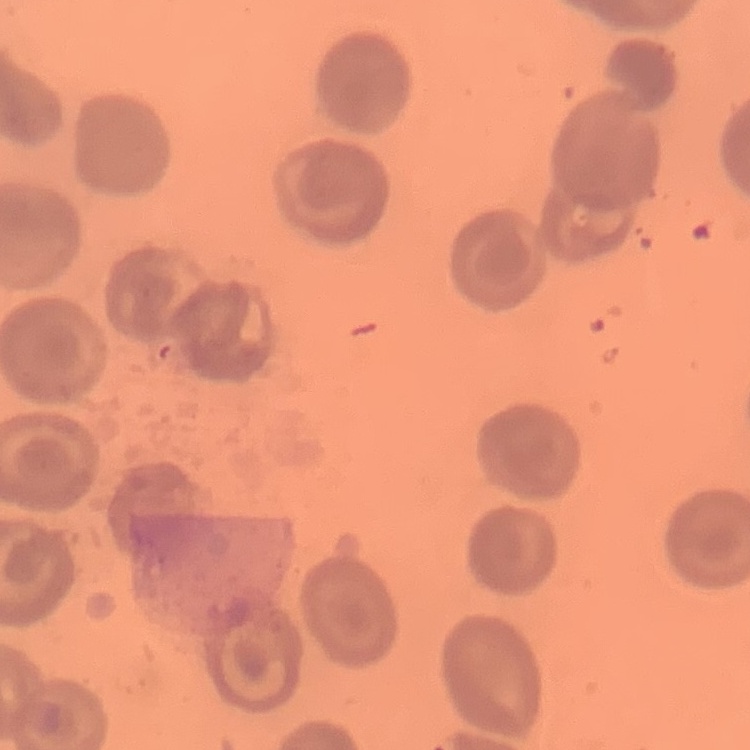

{
  "erythrocyte_morphology": "no rouleaux formation",
  "stain": "Field's or Giemsa",
  "image_type": "one tile cut from a larger photomicrograph",
  "preparation": "thin blood film"
}